Give the extent of all Plasmodium falciparum-infected red blood cells.
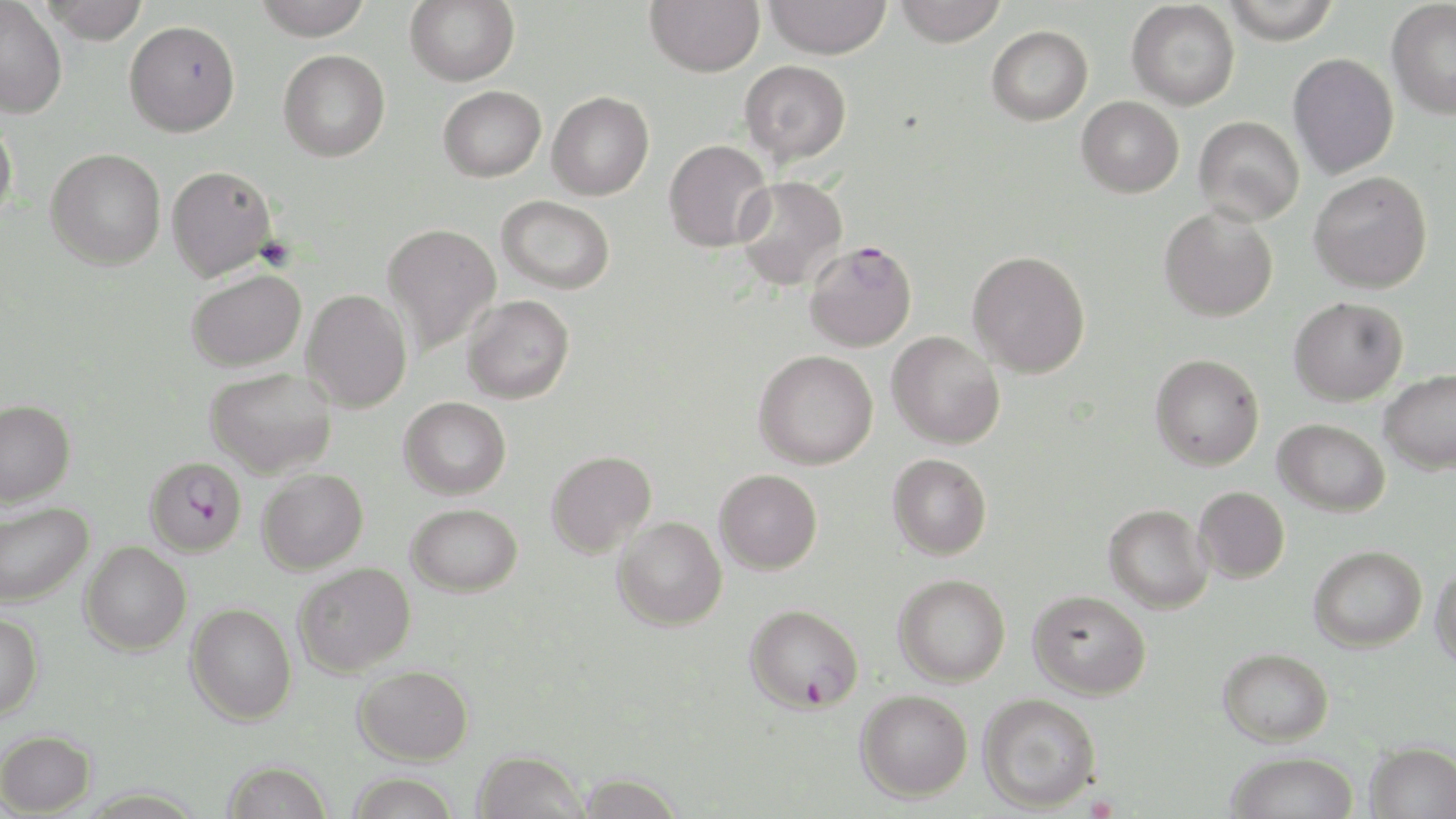
Approximate bounding boxes as (x1,y1)-(x2,y2) corner pairs in pixels.
Plasmodium falciparum-infected red blood cells: (804,241)-(917,352), (144,456)-(247,557), (743,603)-(864,714).

Uninfected red blood cell locations: (43,0)-(149,44), (252,0)-(373,40), (405,0)-(519,86), (645,0)-(765,77), (764,0)-(891,59), (894,0)-(1006,47), (1221,0)-(1341,44), (1387,0)-(1456,119), (0,1)-(68,118), (1126,1)-(1240,110), (124,19)-(240,137), (987,25)-(1093,125), (278,49)-(390,162), (1288,53)-(1399,180), (740,60)-(851,165), (438,85)-(546,181), (547,91)-(654,200), (1076,96)-(1184,197), (1193,115)-(1305,226), (0,116)-(18,227), (663,139)-(774,252), (45,148)-(166,270), (166,165)-(277,281), (1309,171)-(1433,293), (734,176)-(848,292), (496,195)-(615,294), (1158,206)-(1278,322), (382,223)-(502,355), (967,250)-(1090,378), (186,268)-(306,372), (302,289)-(413,413), (462,295)-(575,404), (1288,296)-(1408,405), (887,331)-(1005,449), (753,350)-(878,469), (1149,354)-(1264,471), (205,367)-(337,478), (1379,369)-(1456,474), (399,397)-(511,499), (0,399)-(76,507), (1273,418)-(1390,516), (547,450)-(657,558), (887,453)-(992,559), (257,469)-(368,575), (714,469)-(822,575), (1194,487)-(1290,583), (0,502)-(93,607), (406,503)-(523,597), (1103,504)-(1213,613), (612,516)-(727,631), (80,542)-(191,656), (1309,544)-(1427,652), (294,562)-(415,677), (1431,562)-(1456,671), (893,574)-(1010,687), (1028,589)-(1151,700), (185,603)-(296,726), (0,611)-(44,721), (1218,648)-(1334,746), (353,665)-(473,764), (856,688)-(973,801), (978,693)-(1101,813), (0,729)-(97,816), (1366,741)-(1456,819), (472,749)-(587,819), (1225,751)-(1359,819), (222,760)-(332,819), (576,771)-(684,817), (347,773)-(460,818). Slide-level diagnosis: Plasmodium falciparum. 1000x magnification. Thin blood smear. Single field of view. May-Grünwald-Giemsa-stained preparation. Image is 1456×819 pixels. Light microscopy.